Identify the preparation type.
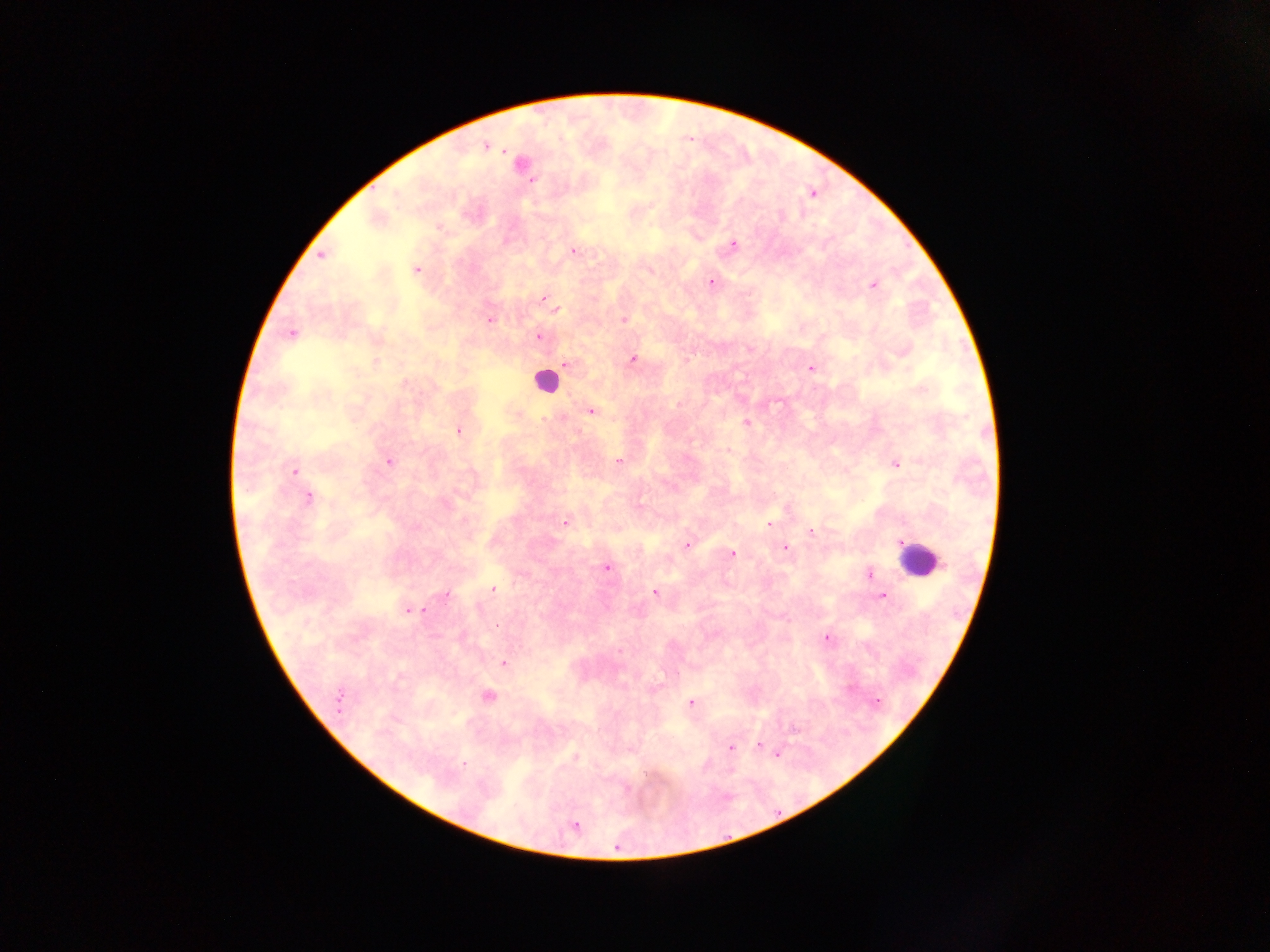

Thick blood smear.

capture = mobile-phone photograph through a microscope
leukocyte locations = approximate centers as [x, y] in pixels: [521, 161], [545, 382], [919, 558]
field of view = single
malaria parasite locations = approximate centers as [x, y] in pixels: [486, 147], [530, 180], [812, 194], [734, 244], [574, 251], [321, 255], [416, 270], [711, 282], [873, 285], [543, 298], [556, 309], [624, 319], [490, 320], [291, 334], [537, 337], [633, 359], [566, 365], [811, 368], [405, 383], [922, 389], [590, 412], [746, 422], [459, 431], [729, 451], [389, 461], [618, 461], [895, 464], [294, 471], [308, 498], [565, 522], [768, 524], [811, 531], [687, 545], [785, 548], [732, 554], [606, 567], [869, 574], [493, 589], [655, 594], [445, 595], [882, 597], [424, 610], [410, 611], [496, 625], [827, 637], [504, 663], [488, 696], [340, 699], [876, 702], [690, 703], [759, 746], [731, 748], [777, 754], [576, 756], [463, 763], [627, 789], [575, 827]
image size = 1270×952 pixels
country = Ghana